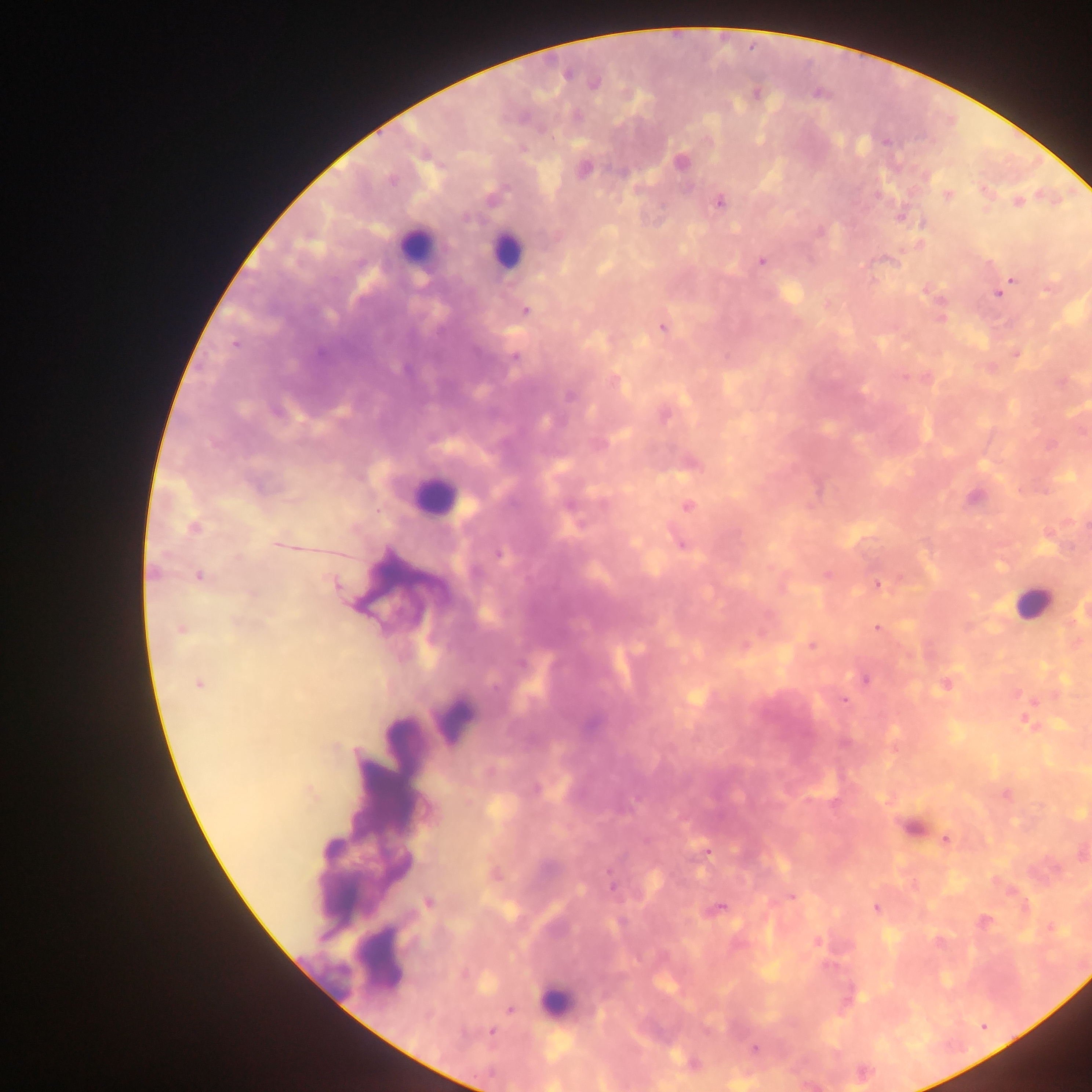
{
  "country": "Ghana",
  "plasmodium_parasite_locations": "approximate centers as x y in pixels: 594 84; 886 142; 680 162; 584 170; 391 181; 947 195; 719 202; 1018 202; 900 217; 467 218; 762 261; 1012 279; 998 293; 525 310; 662 328; 235 345; 1016 354; 515 358; 571 396; 664 416; 256 485; 973 497; 688 506; 571 508; 193 528; 279 544; 682 545; 499 554; 154 572; 827 574; 200 575; 335 584; 878 585; 877 628; 181 629; 812 646; 521 664; 865 679; 198 684; 945 685; 844 701; 535 788; 946 839; 707 852; 611 885; 792 896; 429 903; 720 908; 876 908; 816 941; 510 1010; 492 1032; 754 1049; 693 1063",
  "leukocyte_locations": "approximate centers as x y in pixels: 413 246; 506 250; 434 496; 1030 602; 555 999",
  "capture": "mobile-phone photograph through a microscope",
  "image_size": "1092×1092 pixels",
  "field_of_view": "single",
  "preparation": "thick blood film"
}